Classify this cell by malaria status.
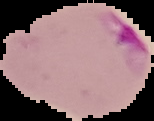
Parasitized.

Image is 154×121 pixels. The area outside the segmented cell region is set to black. From a thin blood film.